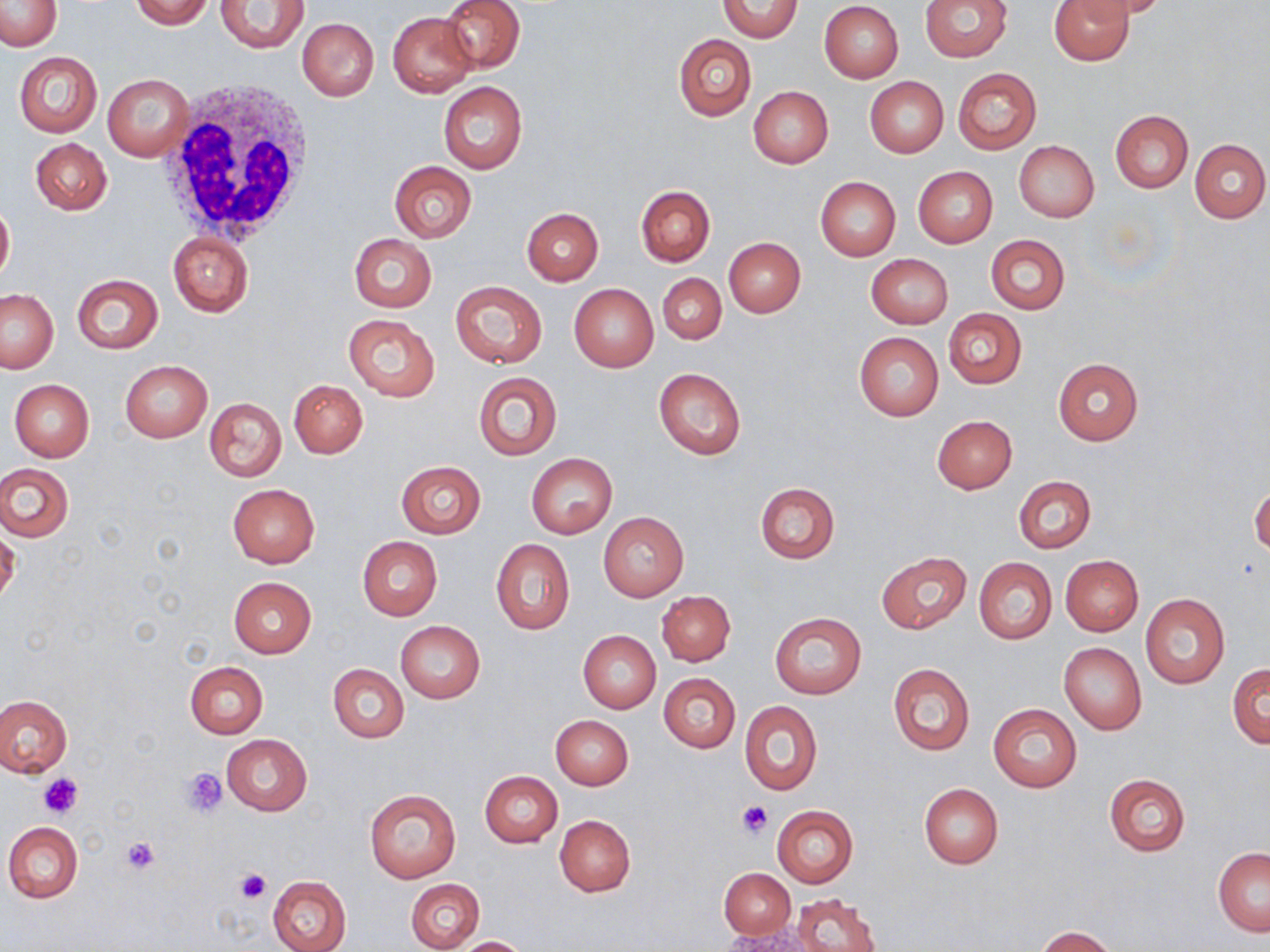

slide-level diagnosis = negative for blood parasites
image size = 1270×952 pixels
modality = light microscopy
platelet locations = approximate bounding boxes as named x1/y1/x2/y2 corners in pixels: (x1=183, y1=768, x2=227, y2=814), (x1=40, y1=774, x2=82, y2=820), (x1=739, y1=801, x2=773, y2=837), (x1=120, y1=836, x2=160, y2=875), (x1=234, y1=867, x2=271, y2=903)
white blood cell locations = approximate bounding boxes as named x1/y1/x2/y2 corners in pixels: (x1=159, y1=81, x2=317, y2=245)
preparation = thin blood smear
stain = May-Grünwald-Giemsa
uninfected red blood cell locations = approximate bounding boxes as named x1/y1/x2/y2 corners in pixels: (x1=0, y1=0, x2=62, y2=50), (x1=129, y1=0, x2=213, y2=29), (x1=440, y1=0, x2=525, y2=73), (x1=717, y1=0, x2=803, y2=41), (x1=921, y1=0, x2=1012, y2=61), (x1=1050, y1=0, x2=1134, y2=65), (x1=1077, y1=0, x2=1172, y2=20), (x1=217, y1=1, x2=309, y2=52), (x1=819, y1=2, x2=904, y2=82), (x1=388, y1=12, x2=477, y2=97), (x1=297, y1=18, x2=379, y2=101), (x1=674, y1=34, x2=756, y2=121), (x1=14, y1=51, x2=103, y2=137), (x1=953, y1=68, x2=1042, y2=153), (x1=103, y1=74, x2=193, y2=161), (x1=866, y1=77, x2=948, y2=158), (x1=438, y1=82, x2=527, y2=175), (x1=748, y1=86, x2=833, y2=168), (x1=1110, y1=110, x2=1193, y2=192), (x1=1190, y1=137, x2=1269, y2=223), (x1=31, y1=139, x2=112, y2=215), (x1=1013, y1=140, x2=1099, y2=222), (x1=390, y1=161, x2=476, y2=242), (x1=913, y1=166, x2=997, y2=248), (x1=815, y1=177, x2=901, y2=261), (x1=636, y1=185, x2=715, y2=266), (x1=0, y1=200, x2=14, y2=284), (x1=520, y1=207, x2=604, y2=285), (x1=167, y1=231, x2=253, y2=317), (x1=349, y1=234, x2=437, y2=313), (x1=985, y1=234, x2=1070, y2=314), (x1=723, y1=237, x2=806, y2=317), (x1=866, y1=253, x2=953, y2=328), (x1=71, y1=273, x2=164, y2=353), (x1=658, y1=273, x2=726, y2=344), (x1=590, y1=276, x2=727, y2=354), (x1=449, y1=280, x2=547, y2=368), (x1=568, y1=283, x2=659, y2=372), (x1=1, y1=288, x2=58, y2=373), (x1=943, y1=308, x2=1026, y2=389), (x1=343, y1=313, x2=440, y2=401), (x1=854, y1=332, x2=943, y2=420), (x1=1053, y1=359, x2=1143, y2=445), (x1=120, y1=360, x2=212, y2=442), (x1=653, y1=367, x2=746, y2=459), (x1=473, y1=372, x2=562, y2=460), (x1=9, y1=379, x2=94, y2=461), (x1=289, y1=379, x2=368, y2=458), (x1=202, y1=397, x2=286, y2=482), (x1=932, y1=415, x2=1017, y2=493), (x1=527, y1=453, x2=617, y2=538), (x1=395, y1=461, x2=486, y2=538), (x1=0, y1=463, x2=73, y2=541), (x1=1013, y1=474, x2=1095, y2=553), (x1=755, y1=481, x2=839, y2=564), (x1=226, y1=484, x2=319, y2=568), (x1=1249, y1=484, x2=1269, y2=557), (x1=598, y1=512, x2=689, y2=602), (x1=0, y1=530, x2=20, y2=606), (x1=357, y1=536, x2=443, y2=620), (x1=491, y1=540, x2=574, y2=635), (x1=876, y1=551, x2=971, y2=634), (x1=1060, y1=554, x2=1143, y2=636), (x1=974, y1=556, x2=1057, y2=644), (x1=228, y1=577, x2=317, y2=657), (x1=656, y1=591, x2=734, y2=665), (x1=1139, y1=592, x2=1230, y2=689), (x1=770, y1=612, x2=867, y2=699), (x1=394, y1=620, x2=486, y2=704), (x1=577, y1=630, x2=661, y2=712), (x1=1060, y1=642, x2=1146, y2=733), (x1=185, y1=661, x2=267, y2=739), (x1=888, y1=662, x2=974, y2=756), (x1=1228, y1=663, x2=1269, y2=747), (x1=329, y1=664, x2=408, y2=742), (x1=659, y1=673, x2=740, y2=752), (x1=0, y1=695, x2=71, y2=777), (x1=740, y1=700, x2=822, y2=795), (x1=988, y1=704, x2=1081, y2=793), (x1=550, y1=715, x2=633, y2=790), (x1=221, y1=733, x2=311, y2=815), (x1=479, y1=770, x2=563, y2=848), (x1=1104, y1=773, x2=1190, y2=856), (x1=919, y1=783, x2=1003, y2=868), (x1=365, y1=788, x2=460, y2=884), (x1=771, y1=806, x2=857, y2=887), (x1=554, y1=815, x2=636, y2=897), (x1=3, y1=822, x2=83, y2=902), (x1=1213, y1=847, x2=1270, y2=935), (x1=720, y1=868, x2=795, y2=939), (x1=267, y1=875, x2=352, y2=952), (x1=406, y1=878, x2=485, y2=952), (x1=793, y1=893, x2=882, y2=952), (x1=1036, y1=926, x2=1117, y2=951), (x1=722, y1=928, x2=818, y2=952), (x1=453, y1=935, x2=529, y2=951)
field of view = single
magnification = 1000x